State which parasite is depicted.
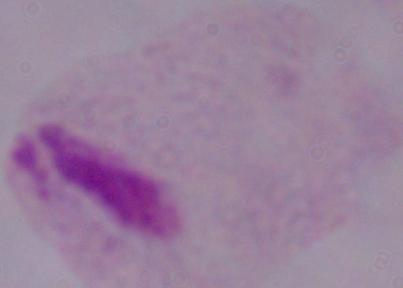

This is a trichomonad.

modality = photomicrograph
magnification = 1000x